Comment on the morphology of the erythrocytes.
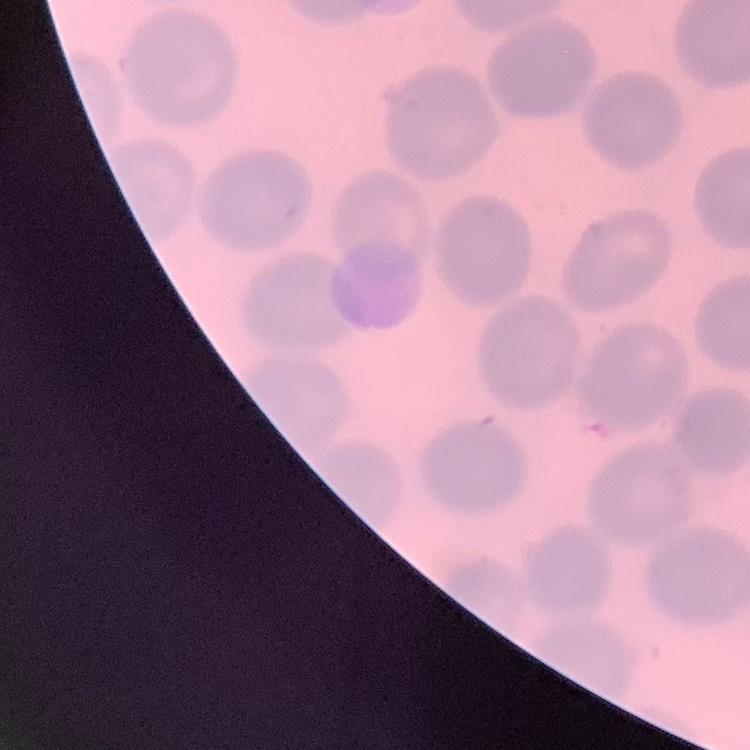

No rouleaux formation.

image_type: one tile cut from a larger photomicrograph
stain: Field's or Giemsa
preparation: thin peripheral smear